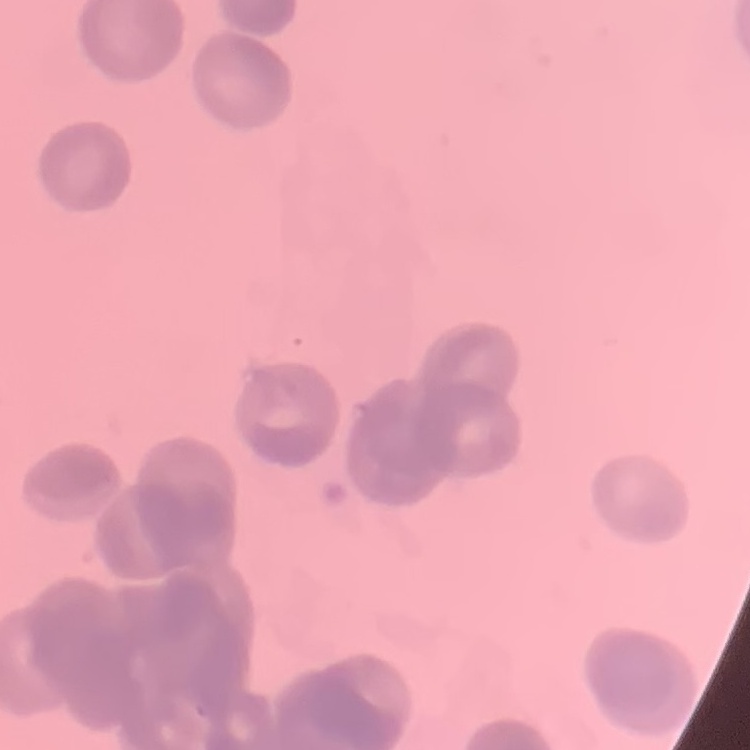 The erythrocytes exhibit rouleaux formation. Thin blood film. One tile cut from a larger photomicrograph. Field's or Giemsa stain.